Point out each Plasmodium parasite.
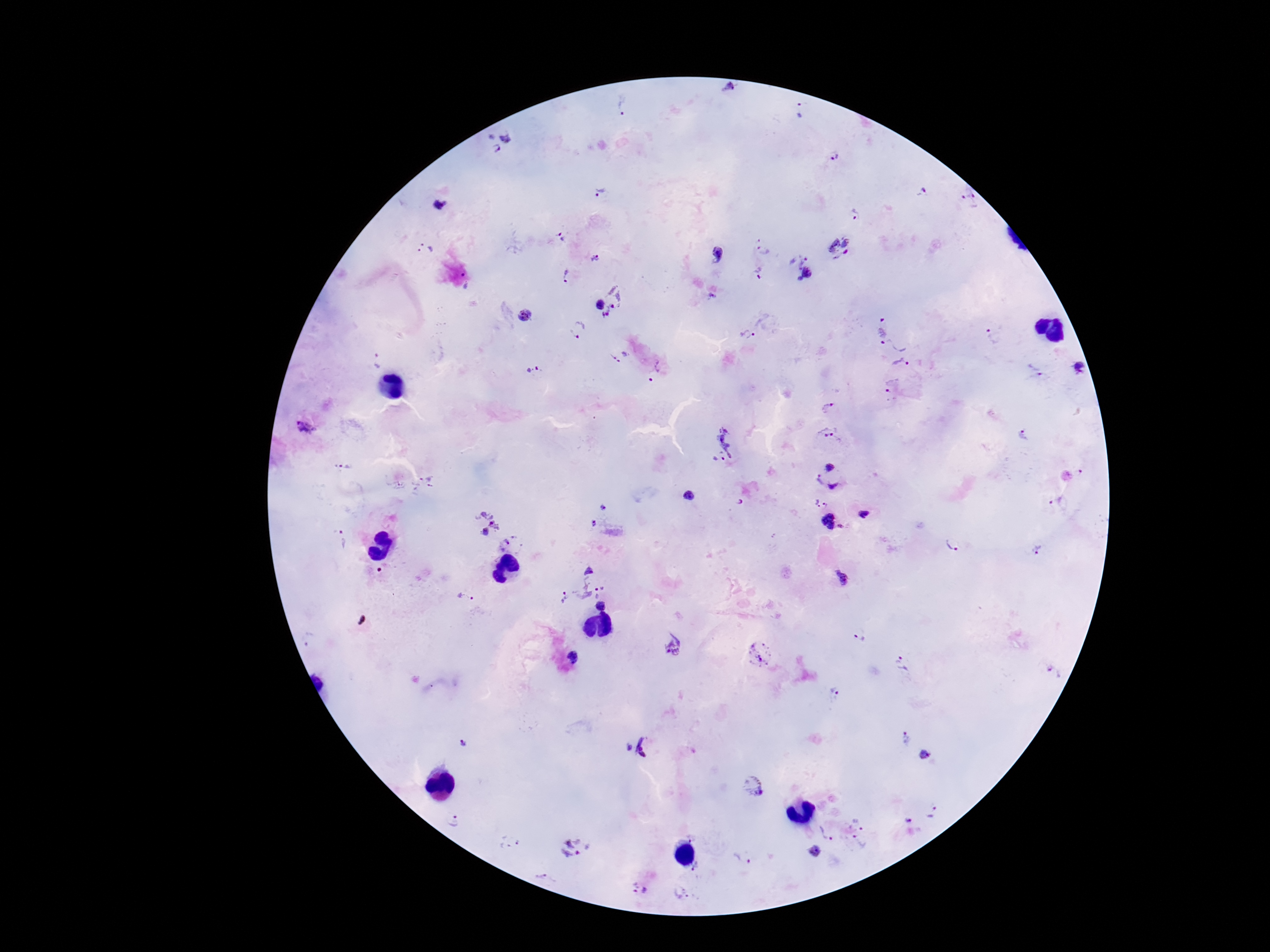

Approximate centers as {x, y} in pixels.
Plasmodium parasites: {730, 92}, {624, 107}, {500, 142}, {835, 155}, {923, 190}, {600, 191}, {968, 198}, {440, 205}, {855, 215}, {561, 237}, {757, 239}, {841, 246}, {424, 250}, {763, 251}, {805, 253}, {718, 254}, {595, 258}, {796, 264}, {808, 272}, {758, 274}, {565, 275}, {466, 280}, {800, 280}, {711, 296}, {609, 301}, {526, 315}, {883, 326}, {577, 331}, {993, 334}, {747, 335}, {899, 339}, {619, 355}, {378, 361}, {902, 368}, {532, 369}, {1078, 369}, {1033, 371}, {656, 372}, {894, 393}, {830, 409}, {306, 428}, {1026, 435}, {829, 439}, {721, 444}, {343, 466}, {830, 466}, {411, 483}, {824, 486}, {688, 496}, {1056, 501}, {814, 502}, {827, 505}, {604, 507}, {864, 513}, {827, 520}, {486, 522}, {593, 524}, {842, 526}, {342, 540}, {953, 540}, {512, 543}, {1038, 550}, {592, 567}, {840, 578}, {578, 591}, {465, 598}, {603, 605}, {860, 637}, {673, 647}, {761, 654}, {573, 657}, {903, 664}, {1054, 671}, {833, 695}, {907, 740}, {463, 744}, {640, 747}, {923, 755}, {753, 787}, {933, 812}, {453, 820}, {908, 820}, {859, 821}, {830, 830}, {693, 835}, {512, 842}, {860, 843}, {575, 847}, {815, 852}, {744, 857}, {700, 868}, {641, 889}, {680, 893}.

patient malaria status = positive
field of view = single
magnification = 100x
stain = Giemsa
capture = smartphone camera through the microscope eyepiece
image size = 1270×952 pixels
preparation = thick peripheral-blood smear